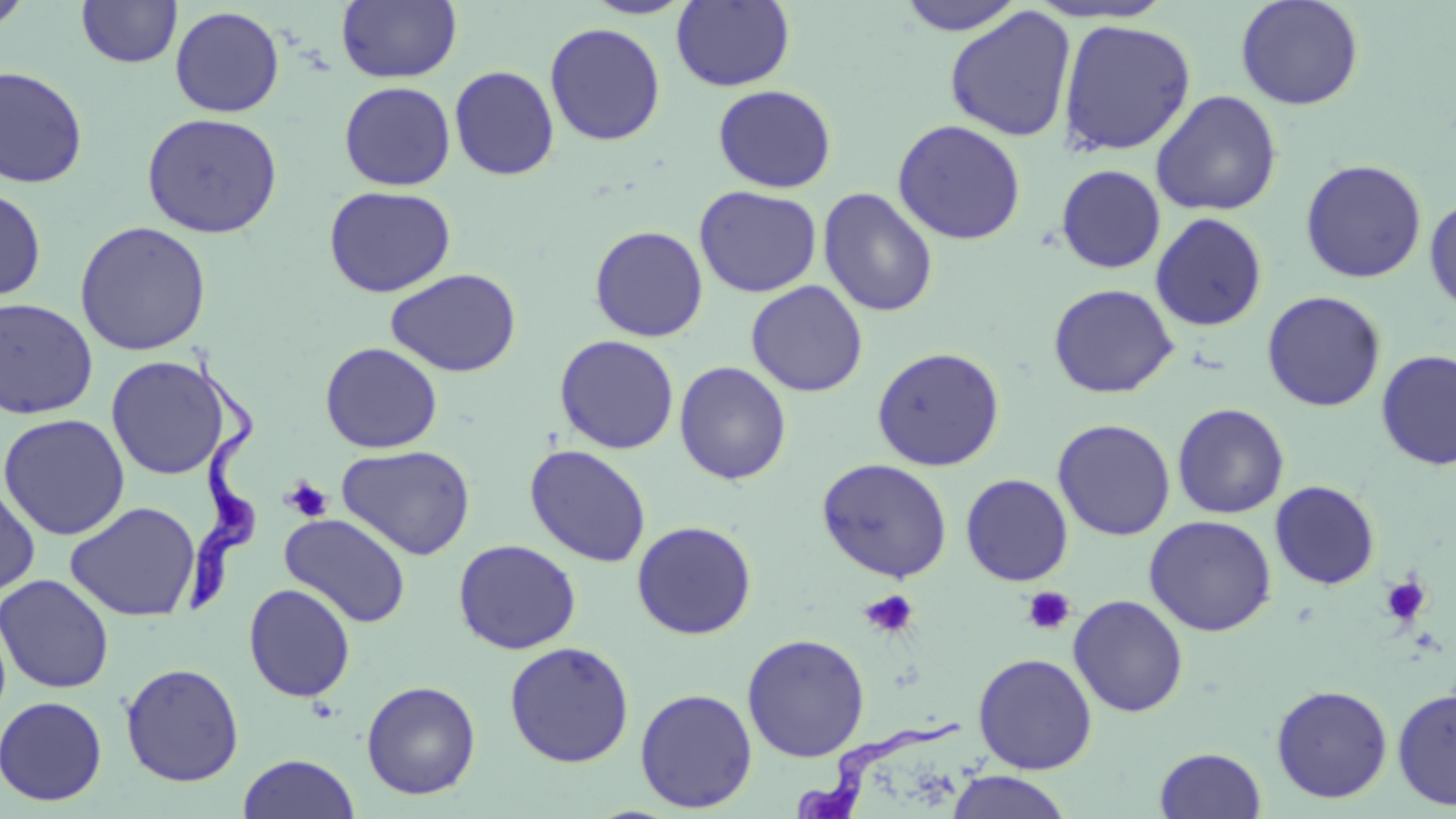

Summary:
  - Coordinate format: approximate bounding boxes as (x1, y1, x2, y2) in pixels
  - Platelet locations: (284, 477, 333, 522), (1380, 574, 1431, 628), (1021, 586, 1076, 635), (860, 589, 919, 639)
  - Uninfected red blood cell locations: (0, 0, 35, 34), (76, 0, 182, 68), (337, 0, 462, 83), (582, 0, 696, 19), (671, 0, 795, 91), (896, 0, 1025, 35), (1235, 0, 1365, 110), (1023, 1, 1174, 24), (170, 5, 285, 118), (944, 7, 1076, 142), (1057, 19, 1196, 156), (544, 22, 666, 146), (0, 65, 89, 189), (449, 65, 560, 180), (339, 81, 456, 191), (712, 85, 837, 193), (1151, 90, 1282, 216), (141, 112, 284, 238), (891, 119, 1027, 245), (1300, 159, 1427, 283), (1055, 164, 1166, 274), (323, 185, 456, 298), (694, 186, 822, 297), (0, 187, 47, 304), (817, 187, 939, 318), (1424, 196, 1456, 315), (1150, 213, 1268, 332), (74, 221, 212, 356), (589, 225, 709, 342), (385, 268, 521, 377), (746, 280, 868, 397), (1047, 283, 1178, 398), (1262, 290, 1386, 412), (0, 297, 99, 419), (554, 334, 679, 454), (320, 342, 442, 453), (871, 346, 1005, 472), (1376, 349, 1455, 470), (105, 355, 232, 480), (674, 361, 792, 485), (1172, 403, 1289, 519), (0, 413, 130, 540), (1052, 418, 1176, 541), (336, 444, 476, 560), (524, 444, 652, 567), (816, 458, 953, 582), (960, 473, 1073, 586), (0, 477, 40, 599), (1269, 480, 1380, 590), (65, 501, 201, 622), (279, 513, 412, 629), (1143, 515, 1277, 636), (631, 520, 757, 640), (453, 539, 581, 654), (0, 573, 114, 694), (243, 583, 356, 702), (1068, 594, 1189, 717), (741, 633, 870, 762), (504, 641, 634, 767), (973, 652, 1097, 774), (120, 662, 244, 787), (361, 680, 481, 799), (1270, 683, 1393, 804), (1392, 686, 1456, 812), (635, 688, 757, 813), (0, 695, 108, 806), (1154, 746, 1267, 819), (236, 753, 360, 819), (945, 771, 1073, 819)
  - Trypanosoma brucei locations: (190, 348, 261, 616), (794, 717, 963, 817)
  - Slide-level diagnosis: Trypanosoma brucei
  - Image size: 1456×819 pixels
  - Magnification: 1000x
  - Preparation: thin blood smear
  - Modality: light microscopy
  - Stain: May-Grünwald-Giemsa
  - Field of view: one of a larger specimen